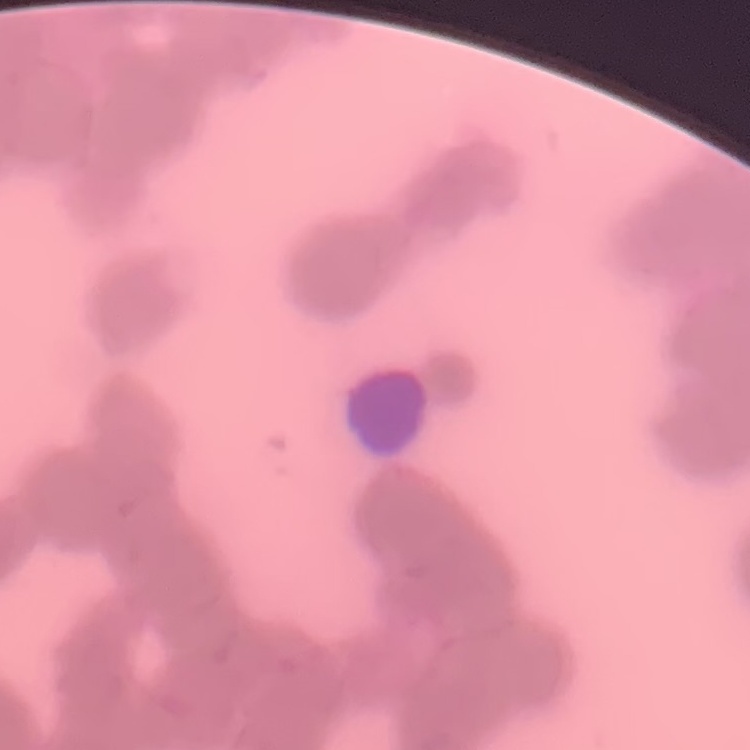 The red blood cells exhibit rouleaux formation. Square crop of a larger photomicrograph. Thin blood smear. Stained with either Field's or Giemsa.